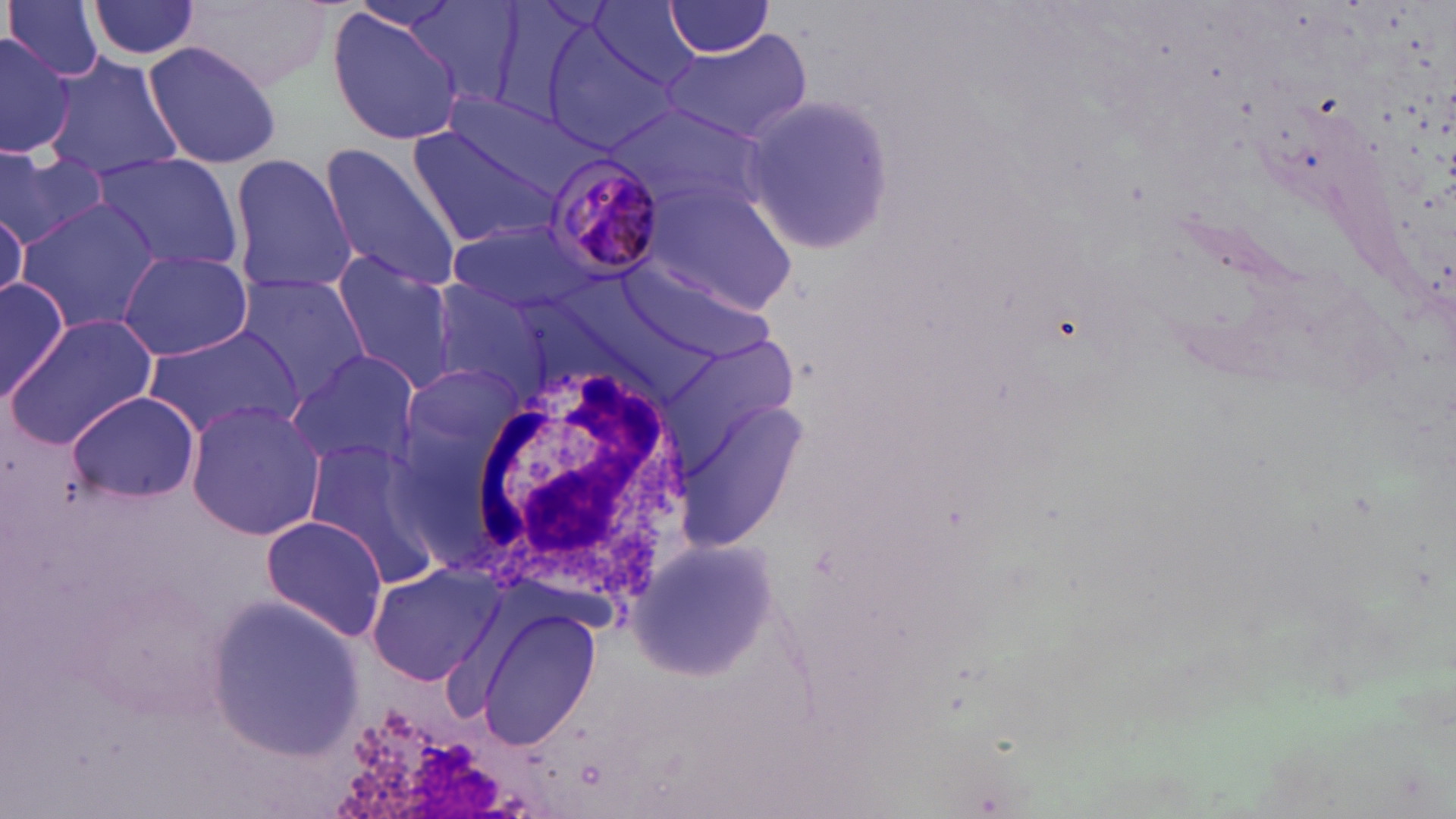
Approximate bounding boxes as (x1, y1, x2, y2) in pixels. White blood cell locations: (466, 358, 695, 605). Plasmodium malariae-infected red blood cell locations: (544, 150, 668, 279). Uninfected red blood cell locations: (5, 0, 107, 83), (87, 0, 204, 61), (184, 0, 334, 88), (663, 1, 777, 57), (402, 2, 529, 108), (588, 2, 702, 94), (327, 8, 464, 144), (543, 27, 683, 152), (0, 29, 72, 158), (660, 30, 811, 145), (142, 40, 283, 171), (41, 53, 183, 179), (433, 89, 601, 207), (738, 92, 898, 254), (405, 118, 574, 250), (319, 140, 462, 292), (0, 150, 110, 249), (87, 152, 245, 276), (229, 155, 357, 296), (646, 183, 799, 316), (16, 199, 163, 334), (0, 205, 26, 311), (447, 217, 599, 314), (119, 252, 256, 361), (331, 252, 457, 391), (624, 264, 776, 365), (232, 271, 371, 400), (0, 277, 70, 404), (420, 279, 550, 395), (6, 314, 158, 450), (142, 324, 304, 441), (286, 351, 421, 471), (406, 364, 528, 468), (65, 390, 200, 504), (677, 400, 805, 546), (185, 402, 327, 540), (301, 437, 444, 584), (260, 514, 389, 641), (627, 534, 776, 682), (364, 563, 504, 685), (207, 596, 363, 760), (477, 607, 601, 754). Slide-level diagnosis: Plasmodium malariae. Image is 1456×819 pixels. One field of a larger specimen. May-Grünwald-Giemsa-stained preparation. Thin blood film. 1000x magnification. Light microscopy.